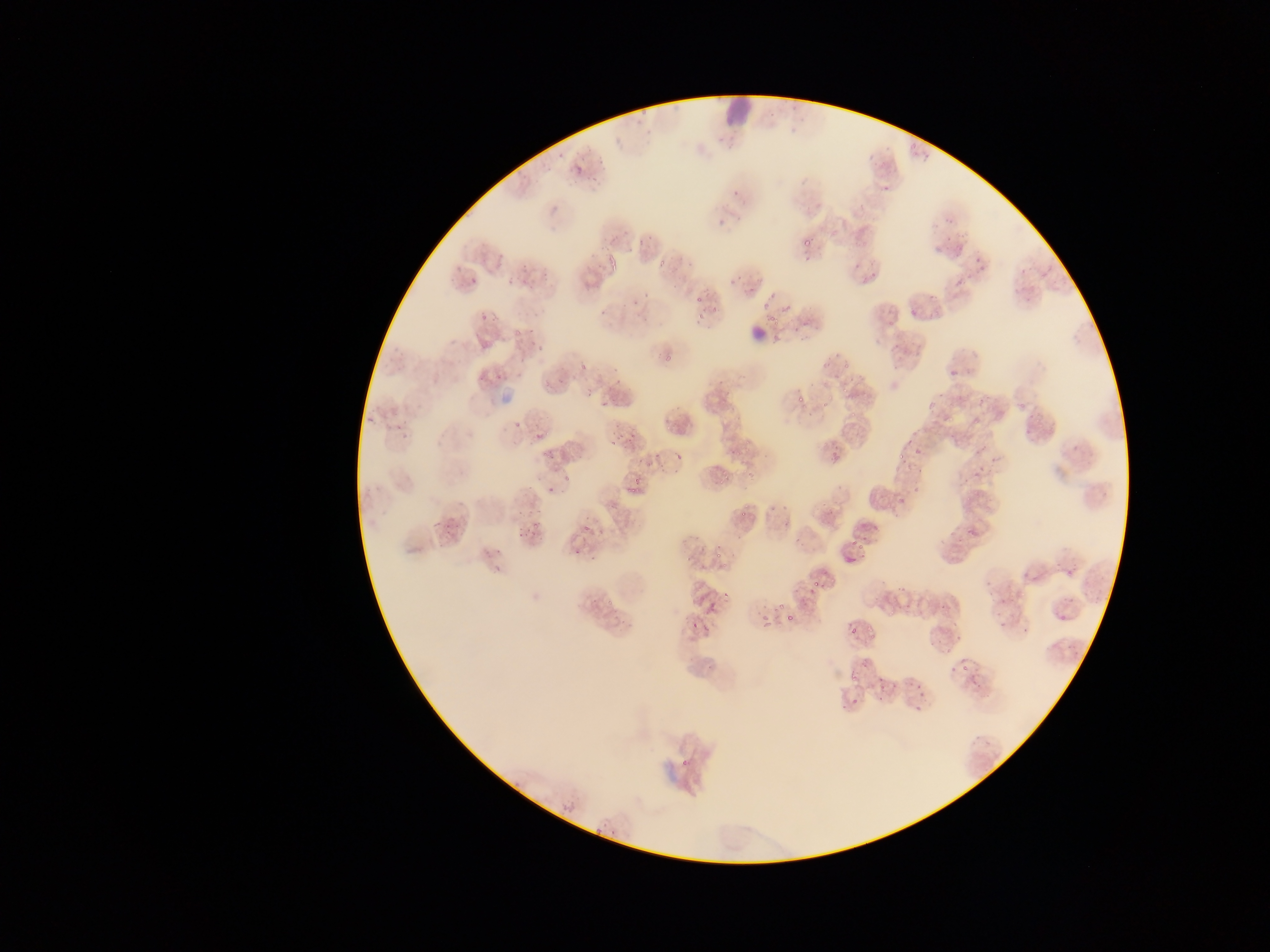
plasmodium_parasite_locations: 'approximate bounding boxes as [left, top, right, bottom] in pixels: [573, 164, 583, 174], [796, 229, 815, 249], [607, 254, 617, 263], [504, 255, 535, 286], [464, 260, 488, 281], [859, 265, 885, 285], [725, 268, 747, 290], [757, 286, 783, 309], [692, 299, 713, 325], [481, 309, 499, 331], [792, 325, 799, 334], [523, 336, 544, 356], [948, 351, 979, 374], [478, 364, 499, 390], [511, 366, 526, 387], [548, 366, 569, 387], [585, 383, 596, 395], [787, 385, 813, 408], [598, 403, 608, 415], [365, 408, 377, 425], [606, 412, 637, 448], [727, 418, 749, 440], [508, 420, 521, 428], [530, 420, 547, 441], [380, 423, 406, 449], [902, 427, 928, 449], [906, 443, 932, 460], [647, 444, 673, 468], [542, 447, 555, 462], [898, 456, 909, 463], [954, 467, 993, 493], [545, 475, 565, 493], [627, 480, 642, 497], [895, 484, 914, 500], [425, 500, 457, 539], [515, 508, 539, 540], [959, 514, 987, 537], [576, 525, 589, 535], [481, 536, 502, 565], [844, 536, 867, 571], [892, 567, 921, 612], [1064, 567, 1077, 579], [991, 572, 1012, 593], [805, 588, 816, 598], [943, 588, 960, 616], [700, 589, 726, 606], [785, 611, 792, 626], [1006, 611, 1019, 630], [755, 613, 768, 633], [846, 620, 863, 634], [684, 621, 701, 638], [945, 646, 974, 669], [846, 666, 867, 678], [969, 675, 986, 694], [878, 679, 895, 698], [840, 684, 866, 714], [905, 688, 926, 715]'
leukocyte_locations: 'approximate bounding boxes as [left, top, right, bottom] in pixels: [722, 94, 756, 127], [748, 324, 765, 343]'
country: Ghana
preparation: thin blood film
image_size: 1270×952 pixels
capture: mobile-phone photograph through a microscope
field_of_view: single